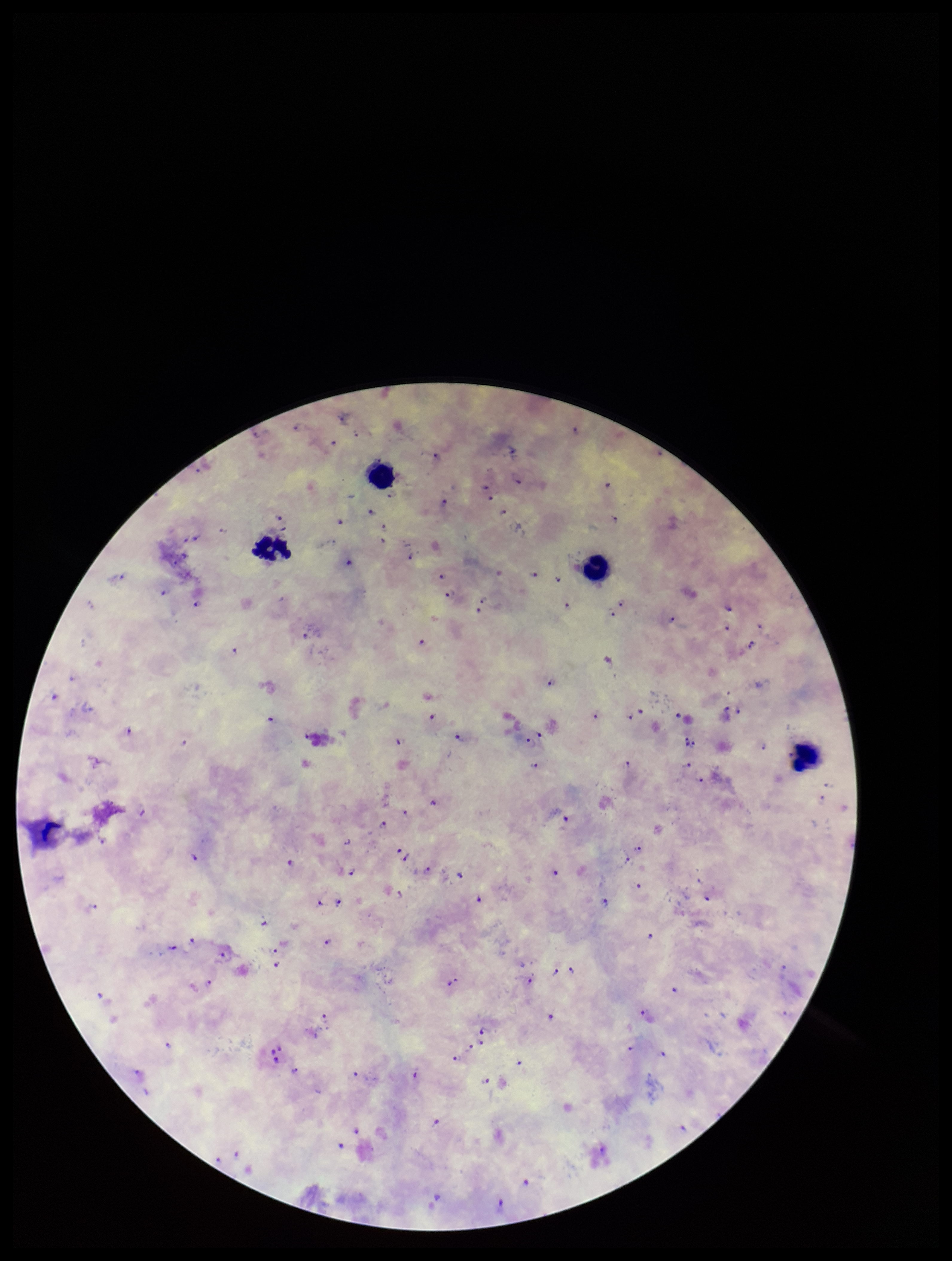 One field from this slide. Parasite count: 109. Plasmodium parasites: seen. Image is 952×1261 pixels. Preparation: thick blood smear. Species reported for this patient: Plasmodium falciparum. Smartphone photograph taken through the eyepiece of a microscope. Patient malaria status: infected. Leukocyte count: 4. Giemsa stain.